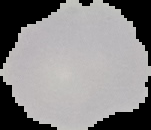
From a thin blood film. Image is 151×130 pixels. Cell region segmented out of the field of view; the surrounding area is masked to black. Malaria status: uninfected.